Name the parasite shown.
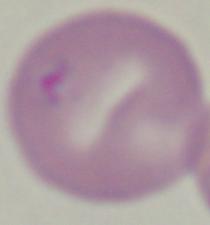
Babesia.

modality: photomicrograph
magnification: 1000x